Assess the morphology of the red blood cells.
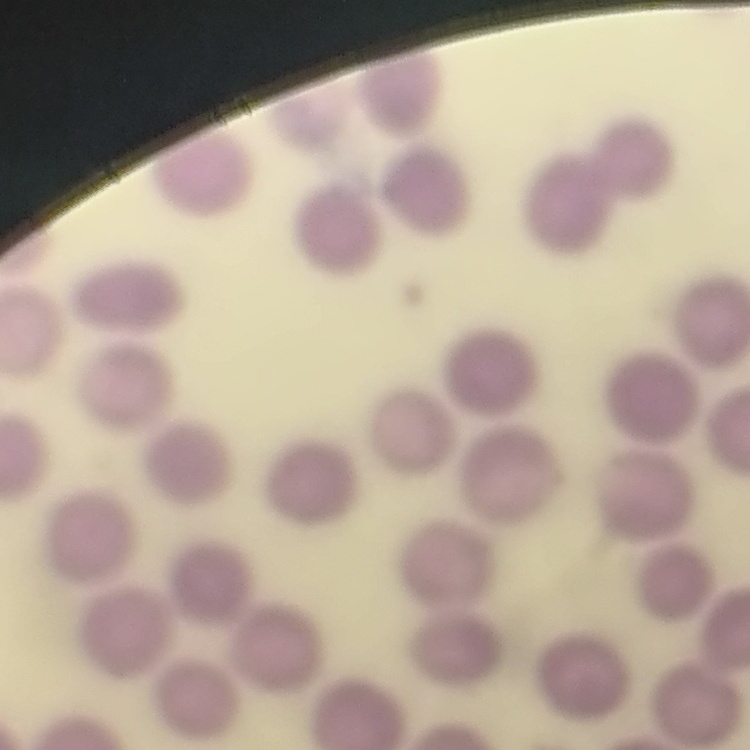
No rouleaux formation.

One tile cut from a larger photomicrograph. Field's or Giemsa stain. Thin blood film.